Point out leukocytes.
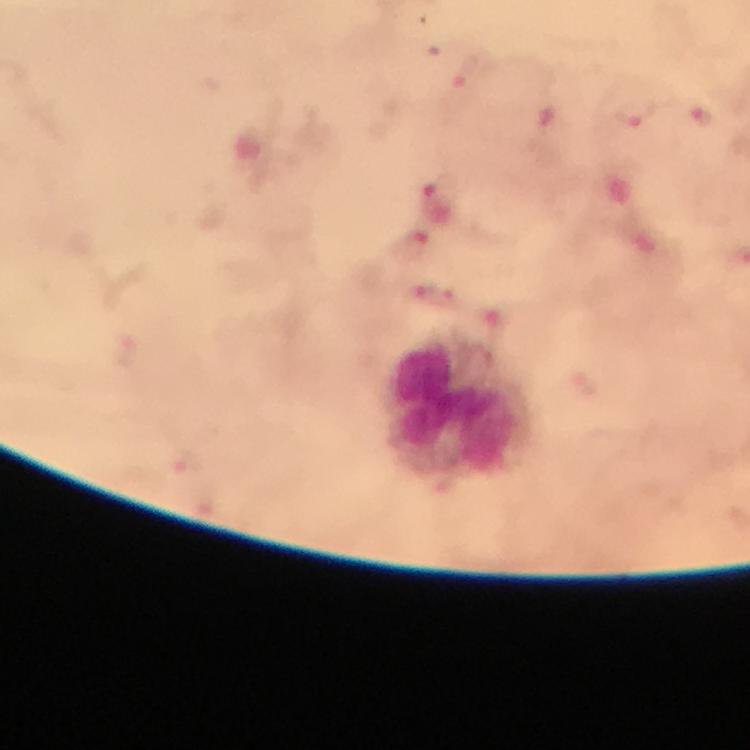

Approximate centers as [x, y] in pixels.
Leukocytes: [460, 408].

Malaria parasite locations: [468, 80], [636, 114], [550, 116], [704, 121], [441, 187], [416, 245], [417, 293], [453, 300]. At 100x magnification. Image is 750×750 pixels. Thick blood smear. Giemsa-stained preparation. From a diagnostic examination for malaria. Photographed through the microscope with a smartphone camera. Immersion oil applied. A crop from one field of view.